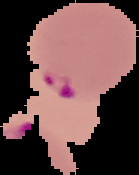

Summary:
  - Image type: cell region segmented out of the field of view; surrounding area masked to black
  - Preparation: thin blood film
  - Result: malaria parasites identified
  - Image size: 139×175 pixels